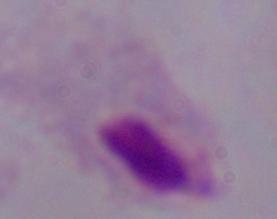 A trichomonad is seen. Micrograph. Captured at 1000x magnification.